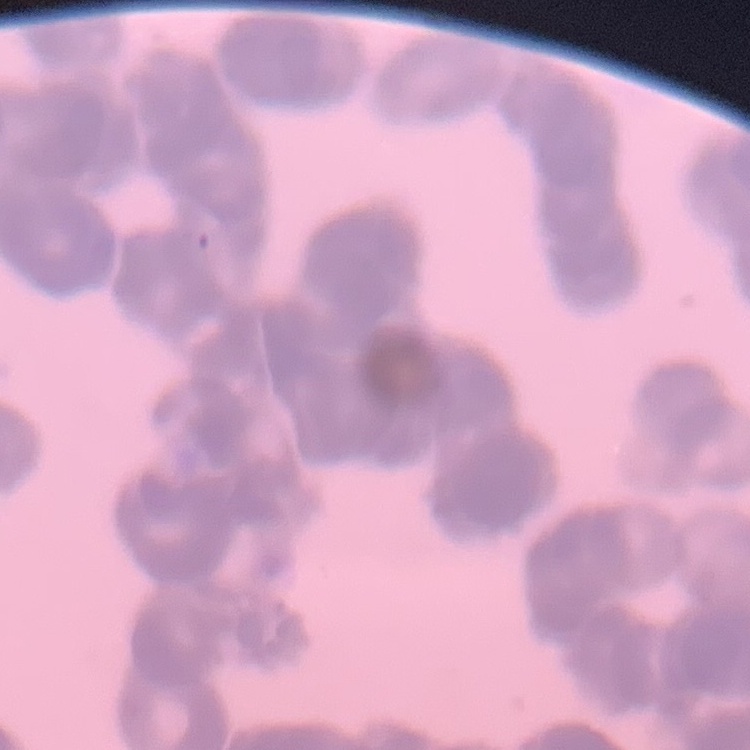 The erythrocytes exhibit rouleaux formation. Stained with either Field's or Giemsa. Thin blood film. Square crop of a larger photomicrograph.